Assess this cell for malaria.
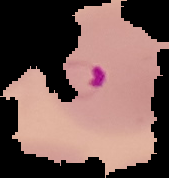

It is parasitized.

From a thin blood film. Image is 169×178 pixels. Cell region segmented out of the field of view; the surrounding area is masked to black.